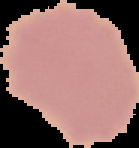

{
  "preparation": "thin blood smear",
  "image_type": "segmented cell region on a black background",
  "image_size": "139×148 pixels",
  "result": "no Plasmodium parasites seen"
}